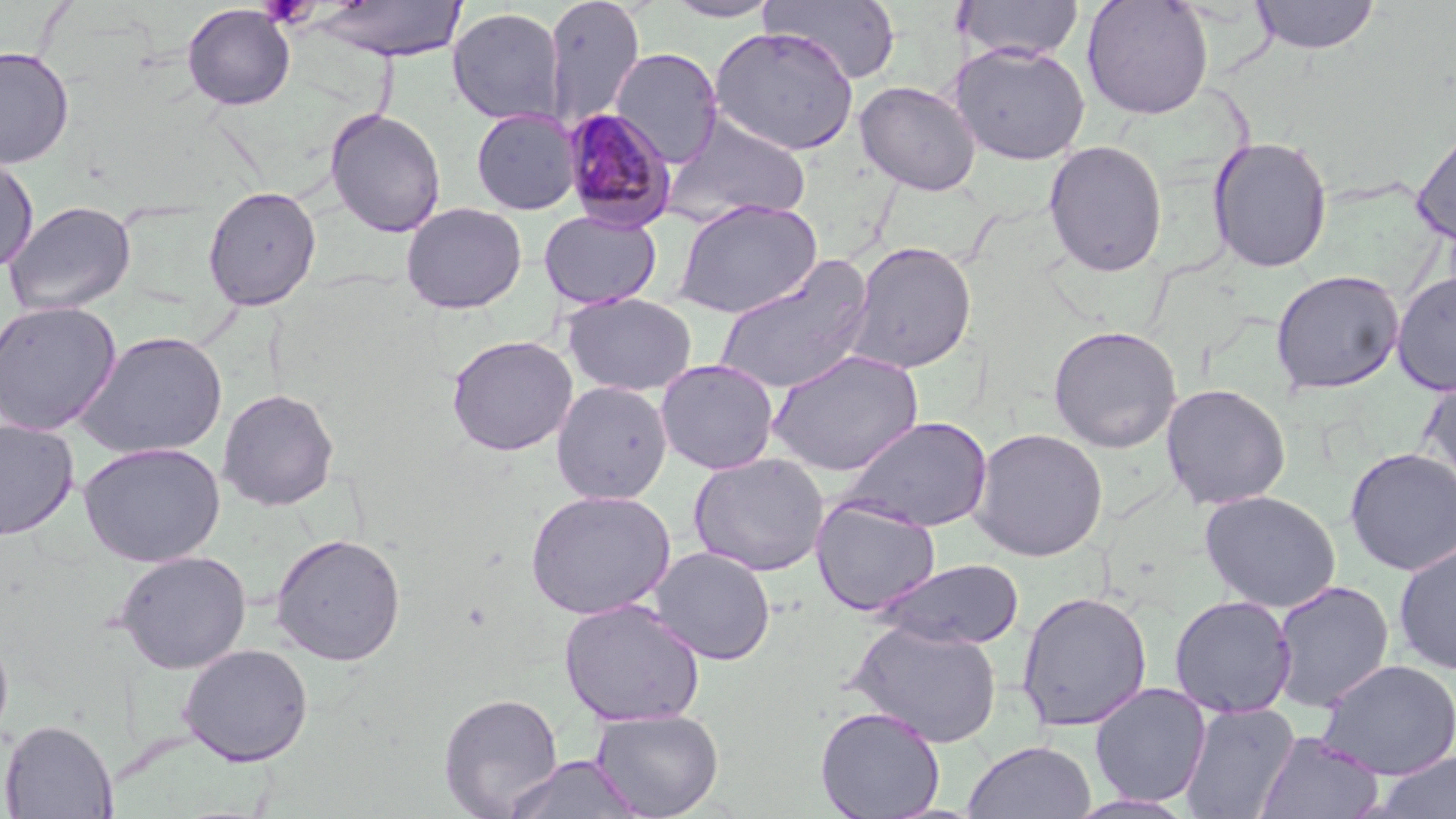 Approximate bounding boxes as named x1/y1/x2/y2 corners in pixels. Platelet locations: (x1=259, y1=0, x2=316, y2=28). Uninfected red blood cell locations: (x1=543, y1=0, x2=645, y2=128), (x1=662, y1=0, x2=782, y2=22), (x1=761, y1=0, x2=902, y2=84), (x1=955, y1=0, x2=1085, y2=62), (x1=1081, y1=0, x2=1214, y2=120), (x1=1250, y1=0, x2=1380, y2=54), (x1=304, y1=1, x2=467, y2=62), (x1=182, y1=4, x2=296, y2=110), (x1=447, y1=7, x2=565, y2=126), (x1=709, y1=26, x2=861, y2=156), (x1=950, y1=42, x2=1091, y2=165), (x1=0, y1=45, x2=75, y2=169), (x1=611, y1=47, x2=723, y2=167), (x1=855, y1=80, x2=981, y2=196), (x1=325, y1=108, x2=447, y2=237), (x1=471, y1=109, x2=581, y2=215), (x1=662, y1=112, x2=813, y2=227), (x1=1411, y1=124, x2=1456, y2=247), (x1=1207, y1=136, x2=1333, y2=274), (x1=1043, y1=139, x2=1168, y2=277), (x1=0, y1=153, x2=39, y2=275), (x1=202, y1=185, x2=322, y2=311), (x1=673, y1=198, x2=822, y2=319), (x1=3, y1=200, x2=137, y2=317), (x1=400, y1=201, x2=528, y2=314), (x1=538, y1=210, x2=662, y2=310), (x1=843, y1=240, x2=978, y2=374), (x1=714, y1=256, x2=876, y2=396), (x1=1270, y1=269, x2=1405, y2=396), (x1=1391, y1=269, x2=1456, y2=396), (x1=561, y1=293, x2=698, y2=396), (x1=0, y1=300, x2=122, y2=436), (x1=1047, y1=324, x2=1182, y2=453), (x1=72, y1=330, x2=228, y2=460), (x1=445, y1=334, x2=578, y2=456), (x1=766, y1=349, x2=924, y2=476), (x1=655, y1=358, x2=779, y2=475), (x1=1419, y1=374, x2=1456, y2=495), (x1=551, y1=380, x2=673, y2=504), (x1=1160, y1=383, x2=1291, y2=510), (x1=217, y1=388, x2=339, y2=511), (x1=836, y1=415, x2=994, y2=533), (x1=1, y1=418, x2=79, y2=540), (x1=969, y1=427, x2=1108, y2=562), (x1=78, y1=441, x2=226, y2=567), (x1=1344, y1=447, x2=1456, y2=576), (x1=689, y1=452, x2=829, y2=577), (x1=524, y1=489, x2=676, y2=620), (x1=1200, y1=490, x2=1341, y2=612), (x1=811, y1=497, x2=941, y2=616), (x1=270, y1=532, x2=407, y2=666), (x1=1393, y1=539, x2=1456, y2=676), (x1=648, y1=547, x2=776, y2=665), (x1=114, y1=550, x2=252, y2=674), (x1=872, y1=558, x2=1025, y2=650), (x1=1270, y1=580, x2=1395, y2=711), (x1=1016, y1=590, x2=1152, y2=732), (x1=1169, y1=595, x2=1296, y2=718), (x1=559, y1=597, x2=705, y2=727), (x1=848, y1=619, x2=1003, y2=748), (x1=0, y1=626, x2=14, y2=747), (x1=178, y1=643, x2=314, y2=766), (x1=1316, y1=658, x2=1456, y2=780), (x1=1089, y1=682, x2=1212, y2=807), (x1=438, y1=692, x2=563, y2=818), (x1=1179, y1=701, x2=1301, y2=818), (x1=814, y1=705, x2=946, y2=819), (x1=590, y1=709, x2=724, y2=818), (x1=1, y1=718, x2=118, y2=818), (x1=1256, y1=731, x2=1384, y2=818), (x1=963, y1=740, x2=1096, y2=819), (x1=1370, y1=752, x2=1456, y2=819), (x1=502, y1=754, x2=644, y2=818), (x1=1066, y1=794, x2=1198, y2=819). Plasmodium malariae-infected red blood cell locations: (x1=561, y1=108, x2=678, y2=232). Slide-level diagnosis: Plasmodium malariae. 1000x magnification. May-Grünwald-Giemsa-stained preparation. Thin blood smear. Optical microscopy. Single field of view. Image is 1456×819 pixels.